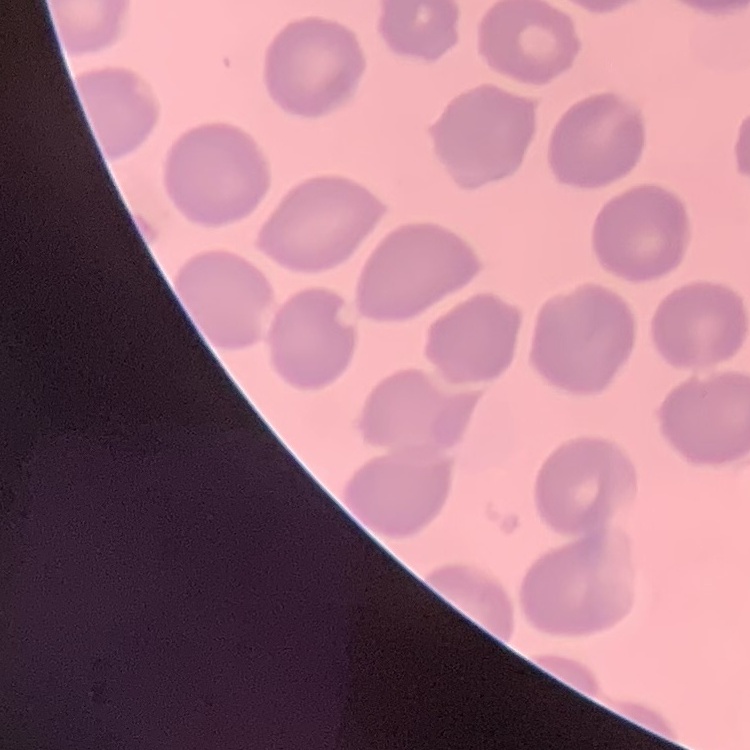
red_blood_cell_morphology: no rouleaux formation
image_type: one tile cut from a larger photomicrograph
preparation: thin peripheral smear
stain: Field's or Giemsa